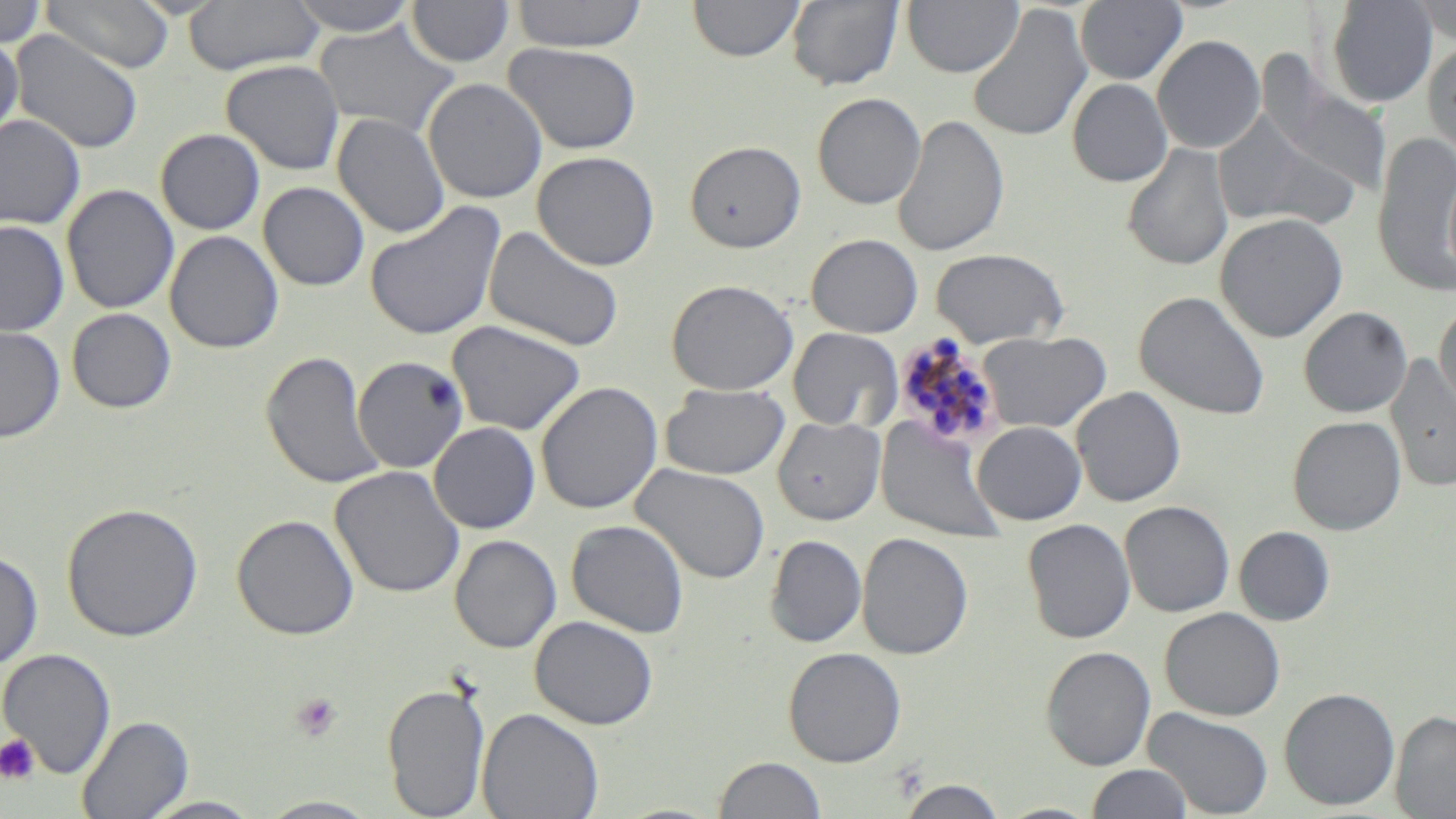

Approximate bounding boxes as [x1, y1, x2, y2] in pixels. Uninfected red blood cell locations: [41, 0, 174, 73], [287, 0, 421, 36], [511, 0, 647, 52], [689, 0, 804, 62], [786, 0, 904, 91], [902, 0, 1023, 77], [1075, 0, 1187, 85], [1326, 0, 1438, 107], [0, 1, 47, 49], [183, 1, 324, 75], [407, 1, 515, 67], [1412, 2, 1456, 43], [966, 5, 1093, 144], [314, 19, 459, 137], [10, 30, 144, 154], [1152, 34, 1266, 154], [0, 35, 23, 145], [1423, 39, 1456, 162], [504, 43, 641, 154], [221, 60, 344, 175], [1262, 76, 1394, 198], [423, 77, 548, 204], [1068, 79, 1172, 187], [812, 92, 927, 209], [1212, 110, 1361, 232], [332, 112, 449, 238], [0, 114, 86, 230], [892, 114, 1009, 258], [156, 128, 265, 235], [1372, 131, 1456, 299], [685, 139, 806, 252], [1122, 143, 1234, 271], [532, 151, 660, 271], [1444, 153, 1456, 287], [259, 181, 369, 291], [61, 184, 179, 314], [364, 201, 506, 341], [1214, 213, 1348, 343], [0, 220, 69, 336], [484, 224, 624, 352], [165, 231, 284, 353], [806, 233, 923, 338], [929, 248, 1070, 348], [666, 279, 798, 396], [1134, 290, 1271, 420], [1435, 302, 1456, 420], [1298, 307, 1412, 418], [66, 308, 176, 413], [446, 320, 587, 435], [0, 325, 65, 442], [787, 327, 903, 431], [976, 331, 1111, 433], [260, 351, 388, 490], [1385, 353, 1456, 492], [352, 356, 469, 473], [535, 381, 663, 514], [659, 383, 790, 480], [1071, 386, 1186, 507], [1287, 415, 1407, 535], [773, 417, 885, 525], [876, 417, 1007, 544], [972, 421, 1086, 525], [429, 422, 540, 534], [630, 463, 771, 584], [330, 466, 465, 598], [61, 501, 203, 642], [1120, 501, 1235, 617], [232, 513, 360, 641], [1022, 518, 1136, 643], [566, 519, 689, 637], [1234, 526, 1335, 626], [857, 532, 973, 660], [449, 534, 562, 653], [765, 535, 866, 648], [0, 550, 44, 670], [1160, 607, 1285, 720], [530, 616, 659, 729], [1041, 646, 1156, 770], [783, 647, 907, 767], [0, 648, 116, 778], [381, 682, 490, 818], [1279, 687, 1401, 810], [1143, 706, 1275, 818], [477, 707, 604, 819], [1390, 709, 1456, 818], [77, 715, 194, 818], [712, 755, 827, 818], [1085, 763, 1195, 819], [897, 778, 1007, 818], [139, 796, 267, 819], [256, 796, 385, 818], [995, 802, 1101, 819]. Platelet locations: [290, 692, 343, 743], [0, 734, 40, 784]. Plasmodium malariae-infected red blood cell locations: [904, 330, 993, 438]. Slide-level diagnosis: Plasmodium malariae. Image is 1456×819 pixels. Thin blood film. May-Grünwald-Giemsa-stained preparation. 1000x magnification. One field of a larger specimen. Light microscopy.